Give the extent of all Babesia divergens-infected red blood cells.
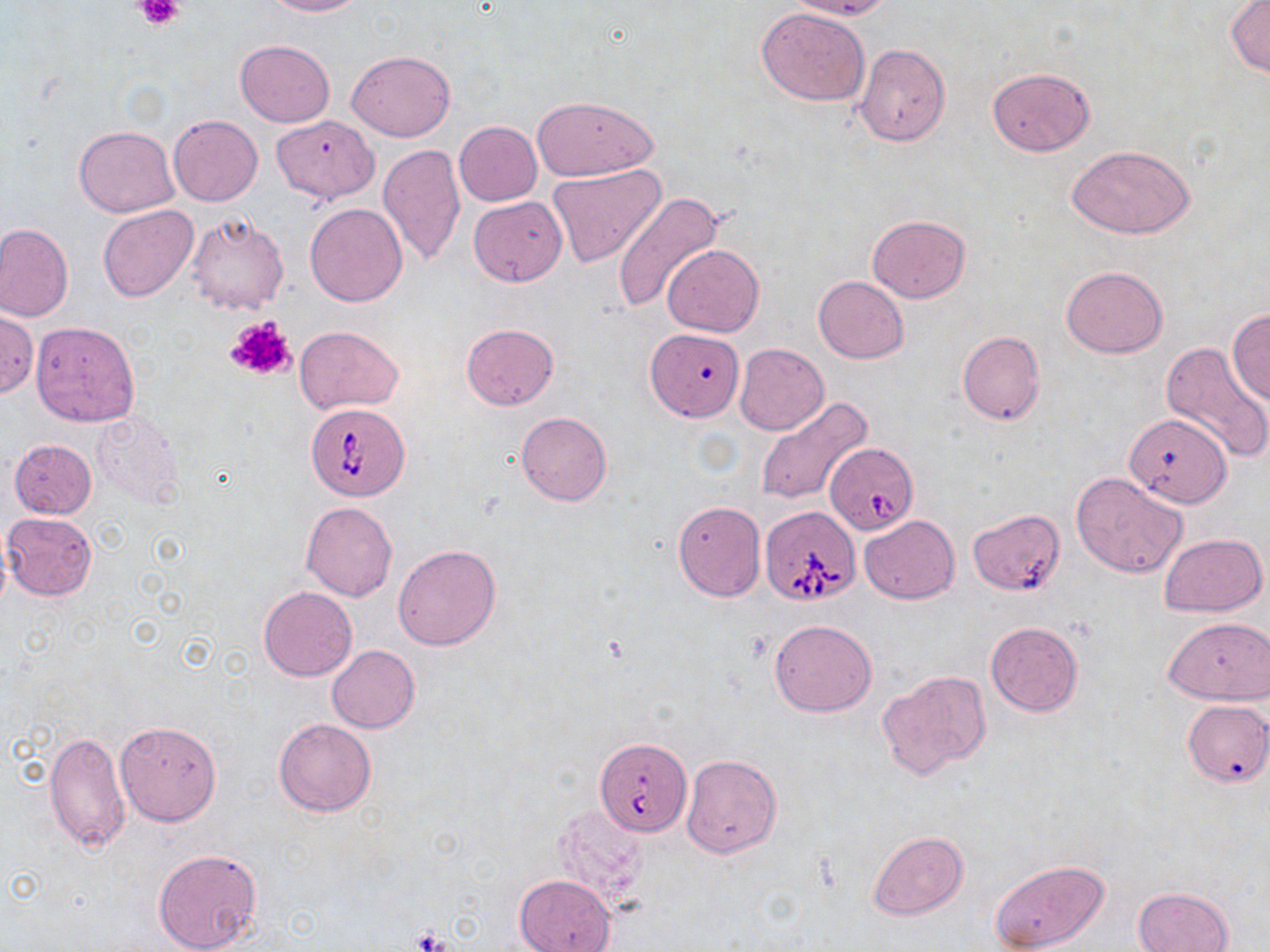
Approximate bounding boxes as [x1, y1, x2, y2] in pixels.
Babesia divergens-infected red blood cells: [306, 403, 411, 501], [824, 443, 919, 533], [760, 506, 860, 606], [595, 738, 691, 834].

Summary:
  - Uninfected red blood cell locations: [263, 0, 364, 16], [784, 0, 892, 21], [1226, 0, 1269, 76], [757, 7, 870, 106], [234, 40, 335, 127], [855, 44, 950, 145], [348, 50, 454, 142], [986, 66, 1095, 156], [532, 95, 657, 179], [169, 115, 263, 207], [271, 115, 379, 204], [453, 121, 542, 206], [74, 125, 179, 216], [376, 144, 465, 266], [1067, 144, 1197, 239], [547, 164, 666, 268], [614, 191, 723, 314], [470, 197, 566, 285], [305, 201, 408, 305], [98, 205, 199, 301], [185, 213, 289, 315], [867, 214, 971, 303], [0, 223, 73, 322], [662, 243, 763, 337], [1060, 267, 1169, 358], [813, 277, 908, 364], [1227, 309, 1270, 404], [0, 311, 38, 398], [29, 321, 140, 427], [461, 323, 558, 409], [295, 326, 404, 413], [648, 329, 746, 426], [957, 331, 1046, 424], [1161, 341, 1270, 463], [735, 343, 829, 436], [755, 396, 873, 507], [516, 411, 612, 506], [91, 413, 185, 508], [9, 439, 97, 519], [1072, 472, 1188, 578], [672, 499, 766, 602], [301, 501, 397, 601], [967, 507, 1066, 595], [2, 512, 97, 600], [860, 515, 959, 605], [1160, 532, 1267, 617], [392, 545, 501, 651], [258, 586, 356, 681], [1164, 617, 1270, 705], [769, 619, 878, 717], [985, 621, 1083, 718], [326, 645, 420, 732], [877, 670, 992, 780], [1182, 699, 1270, 788], [273, 717, 378, 817], [115, 720, 222, 826], [45, 730, 130, 852], [680, 752, 782, 859], [868, 831, 967, 919], [153, 848, 263, 952], [989, 858, 1109, 951], [514, 874, 616, 952], [1133, 887, 1234, 952]
  - Platelet locations: [138, 0, 182, 29], [224, 314, 297, 381], [412, 929, 457, 952]
  - Slide-level diagnosis: Babesia divergens
  - Image size: 1270×952 pixels
  - Preparation: thin blood smear
  - Stain: May-Grünwald-Giemsa
  - Modality: light microscopy
  - Field of view: one of a larger specimen
  - Magnification: 1000x